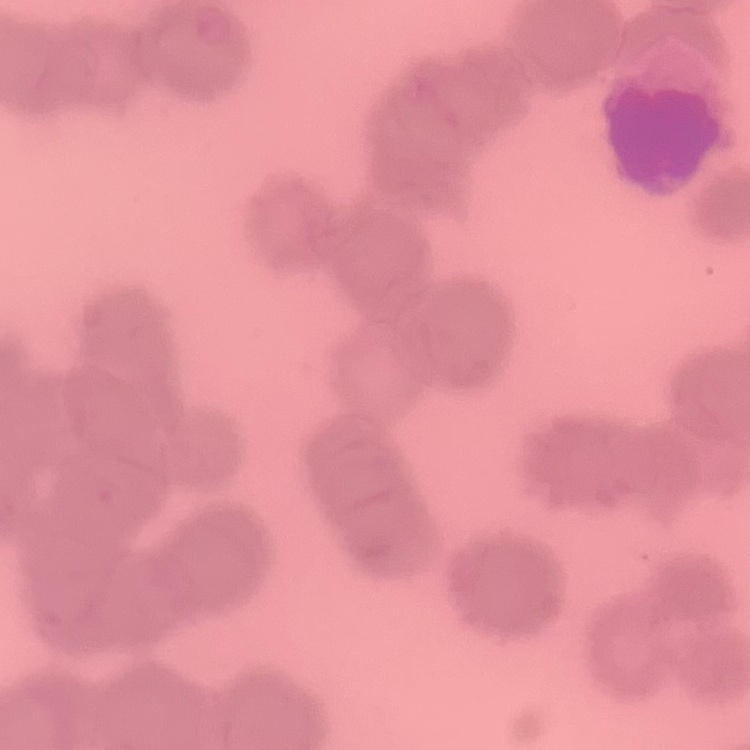

erythrocyte_morphology: rouleaux formation
image_type: square crop of a larger photomicrograph
preparation: thin peripheral smear
stain: Field's or Giemsa